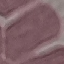

{
  "malaria_status": "uninfected",
  "image_type": "automatically extracted cell patch, resized to 64 × 64 pixels",
  "capture": "smartphone camera at the microscope eyepiece",
  "stain": "Giemsa",
  "preparation": "thin blood smear"
}